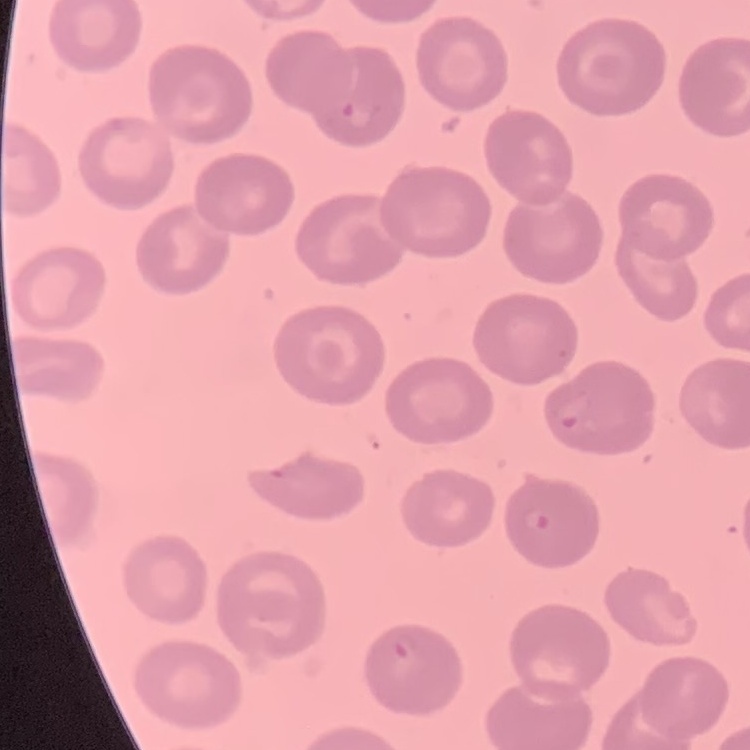
Summary:
  - Red blood cell morphology: no rouleaux formation
  - Stain: Field's or Giemsa
  - Image type: one tile cut from a larger photomicrograph
  - Preparation: thin peripheral smear